Point out each Plasmodium parasite.
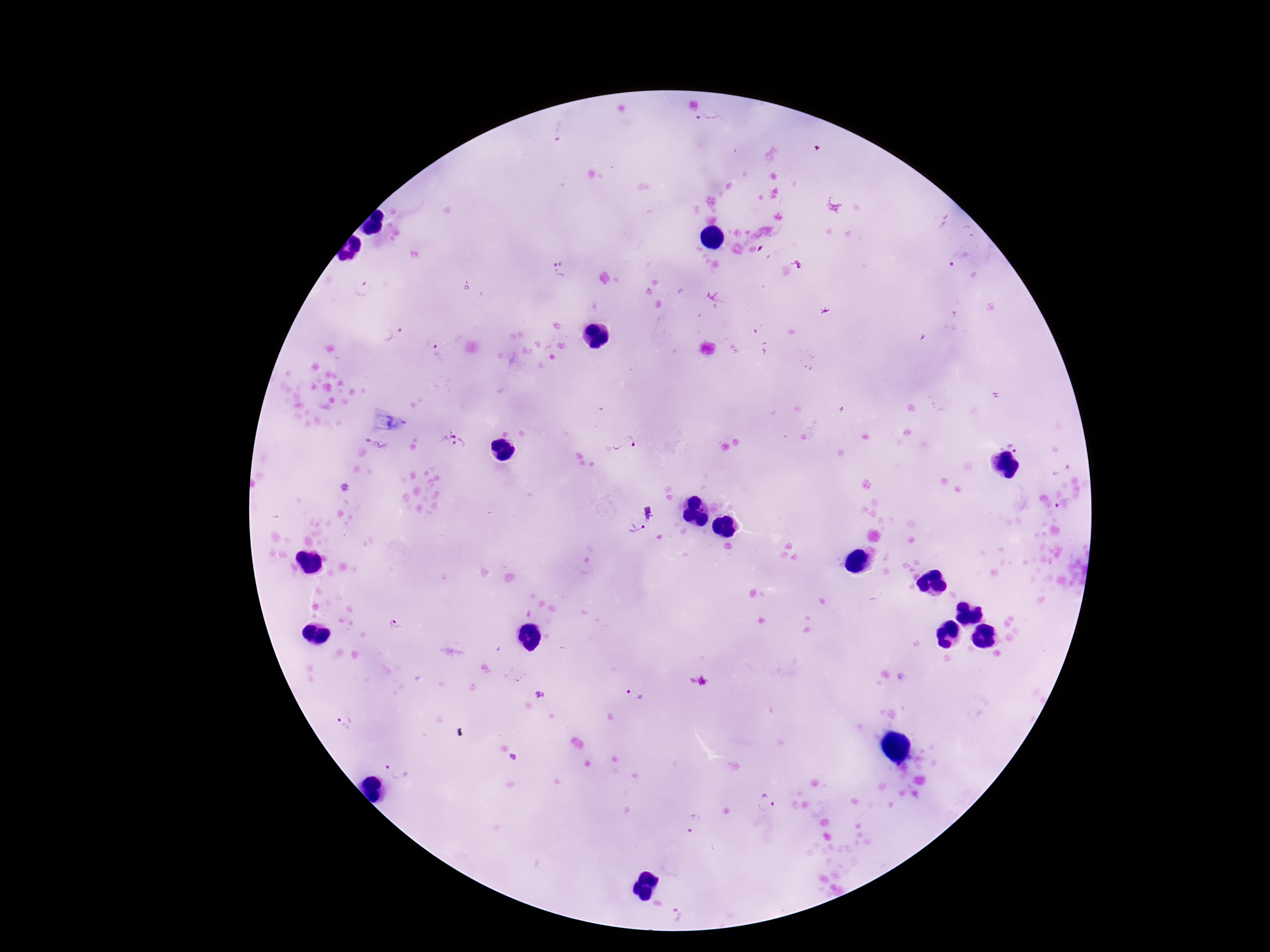

Approximate centers as [x, y] in pixels.
Plasmodium parasites: [706, 120], [561, 130], [956, 258], [559, 269], [394, 333], [438, 353], [453, 442], [626, 442], [1017, 442], [375, 443], [1063, 507], [649, 513], [636, 528], [637, 693], [344, 721], [396, 769], [764, 801], [694, 823], [678, 912].

Patient malaria status: infected. 100x magnification. Image is 1270×952 pixels. Single field of view. Giemsa-stained preparation. Smartphone photograph taken through the microscope eyepiece. Thick peripheral-blood smear.